Look for Plasmodium parasites.
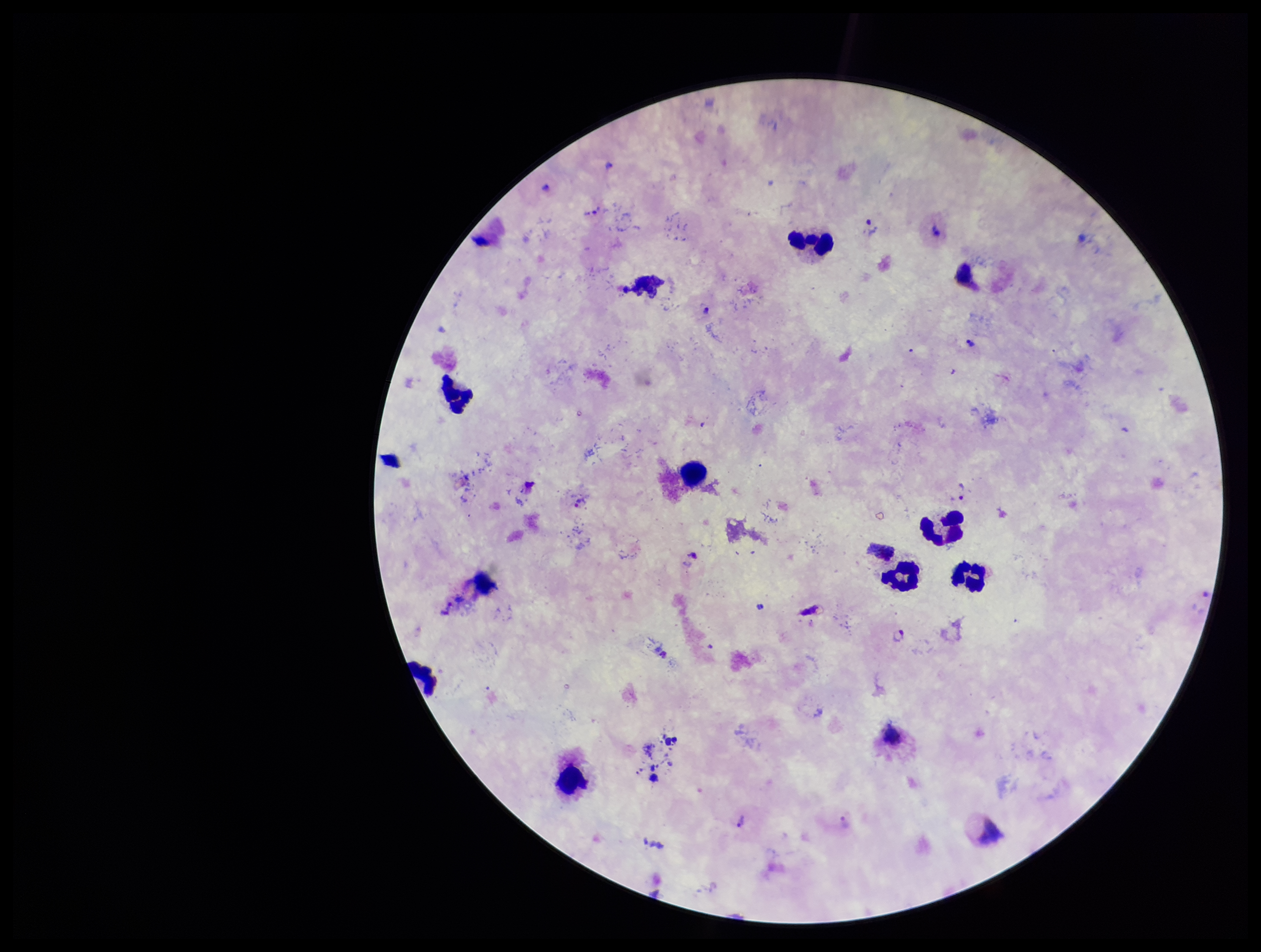
Seen.

Summary:
  - Species reported for this patient: Plasmodium vivax
  - Image size: 1261×952 pixels
  - Leukocyte count: 8
  - Parasite count: 5
  - Preparation: thick blood smear
  - Capture: smartphone photograph through the microscope eyepiece
  - Field of view: single
  - Stain: Giemsa
  - Patient malaria status: positive